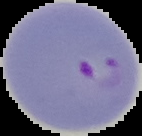

Image is 142×136 pixels. Malaria status: parasitized. The area outside the segmented cell region is set to black. From a thin blood smear.